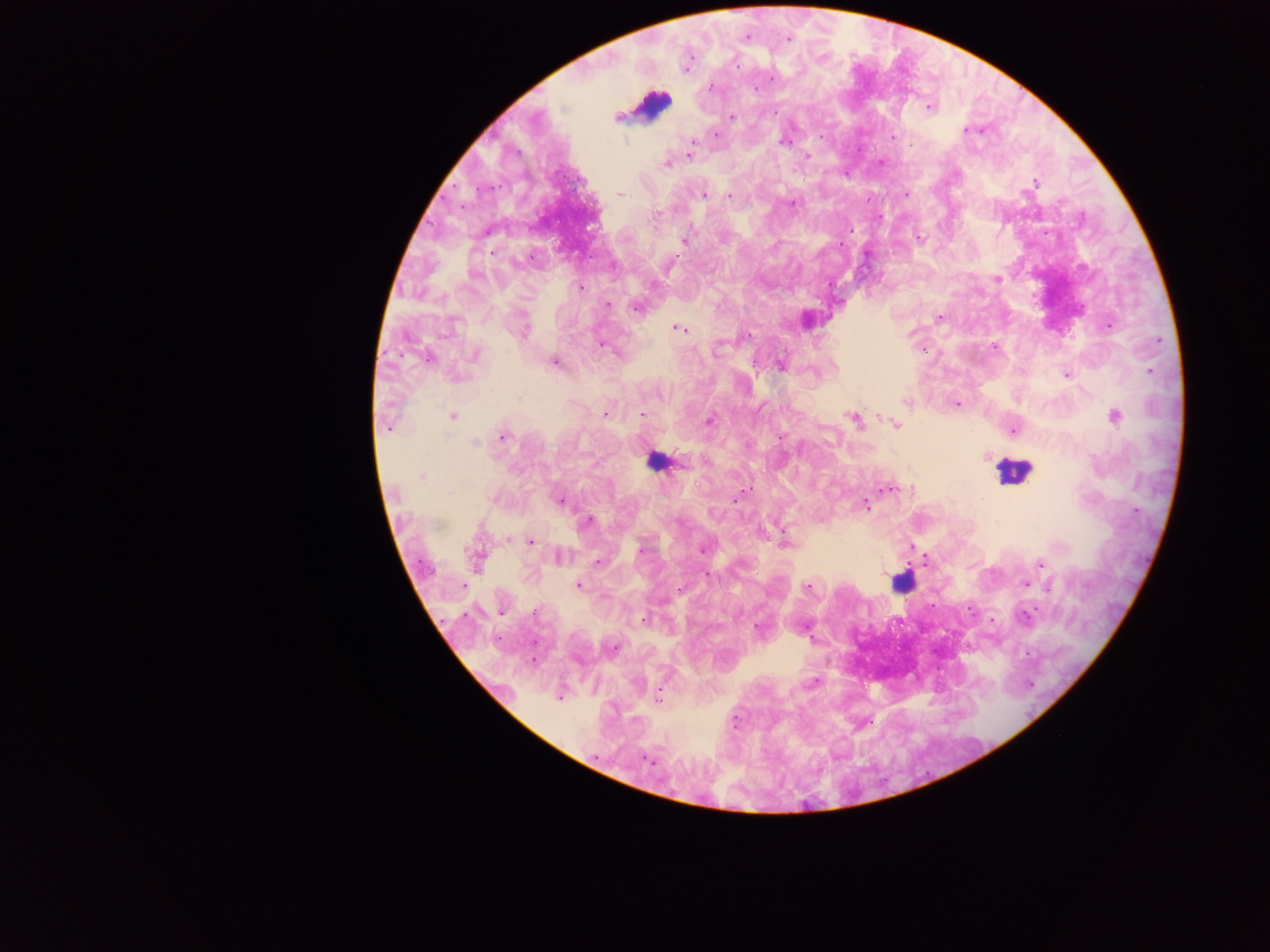
leukocyte locations = approximate centers as (x, y) in pixels: (650, 106), (656, 460), (1012, 470), (901, 581)
capture = mobile-phone photograph through a microscope
image size = 1270×952 pixels
malaria parasite locations = approximate centers as (x, y) in pixels: (745, 37), (788, 39), (687, 64), (755, 89), (928, 107), (731, 116), (616, 117), (964, 130), (716, 134), (822, 138), (892, 138), (783, 140), (689, 155), (806, 155), (881, 162), (667, 163), (845, 172), (1035, 182), (620, 194), (906, 194), (703, 195), (729, 196), (792, 202), (877, 217), (919, 238), (684, 240), (841, 244), (997, 279), (581, 288), (606, 305), (637, 306), (940, 317), (1109, 325), (522, 329), (678, 329), (747, 336), (602, 344), (995, 346), (475, 353), (427, 358), (554, 362), (781, 365), (1066, 374), (456, 378), (908, 401), (957, 404), (605, 414), (641, 415), (452, 416), (1113, 416), (852, 418), (709, 421), (895, 425), (1013, 428), (503, 437), (780, 438), (884, 489), (735, 499), (561, 500), (865, 505), (587, 521), (785, 541), (530, 542), (911, 545), (704, 547), (558, 556), (476, 558), (598, 561), (925, 561), (1040, 564), (708, 574), (1026, 583), (577, 585), (808, 587), (680, 589), (932, 607), (757, 629), (813, 681), (559, 696), (658, 697), (647, 759)
field of view = single
preparation = thick blood film
country = Ghana